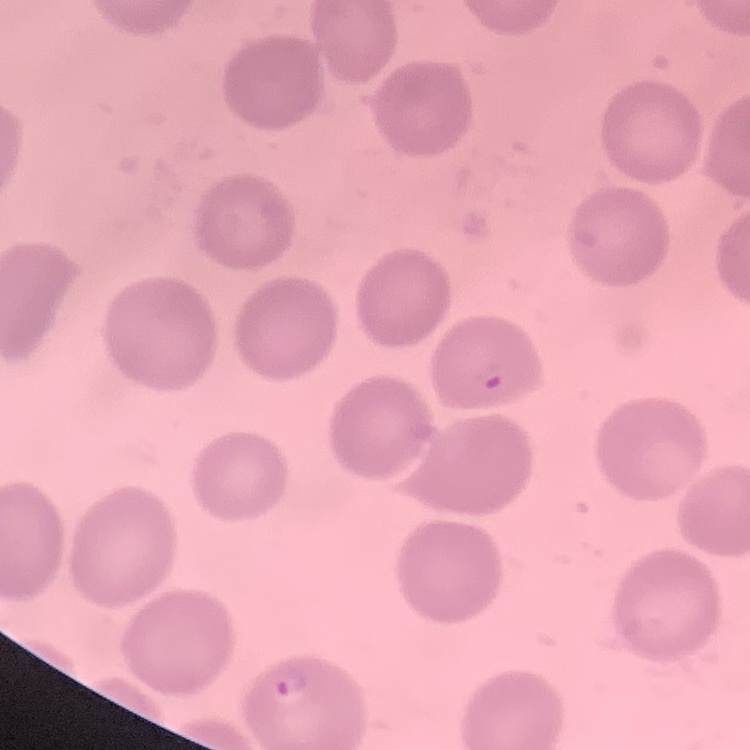
red blood cell morphology = no rouleaux formation
preparation = thin peripheral smear
image type = square crop of a larger photomicrograph
stain = Field's or Giemsa